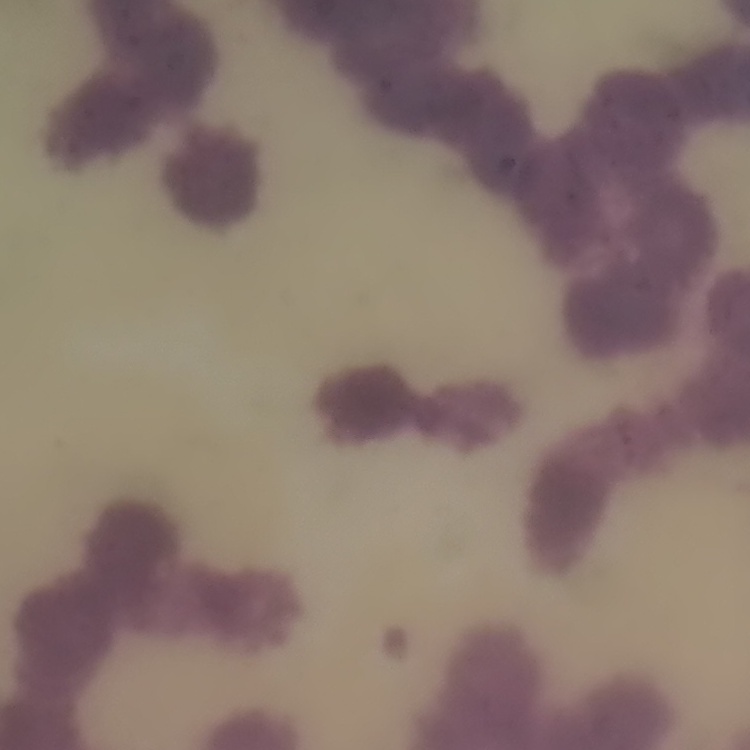

{
  "erythrocyte_morphology": "rouleaux formation",
  "preparation": "thin peripheral smear",
  "stain": "Field's or Giemsa",
  "image_type": "one tile cut from a larger photomicrograph"
}